Identify the parasite.
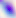
Toxoplasma gondii.

{
  "modality": "photomicrograph",
  "magnification": "400x"
}